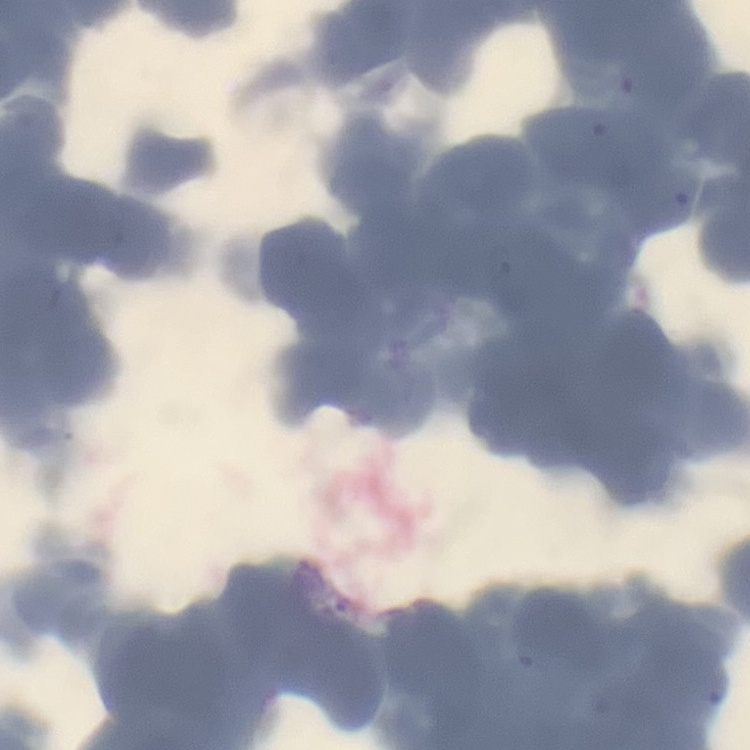

erythrocyte morphology = rouleaux formation
image type = one tile cut from a larger photomicrograph
stain = Field's or Giemsa
preparation = thin blood film